Assess this cell for malaria.
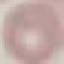
Uninfected.

capture = smartphone camera at the microscope eyepiece
stain = Giemsa
image type = automatically extracted cell patch, resized to 64 × 64 pixels
preparation = thin blood smear